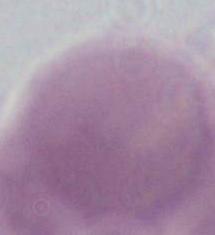

modality = photomicrograph
identification = red blood cell
magnification = 1000x